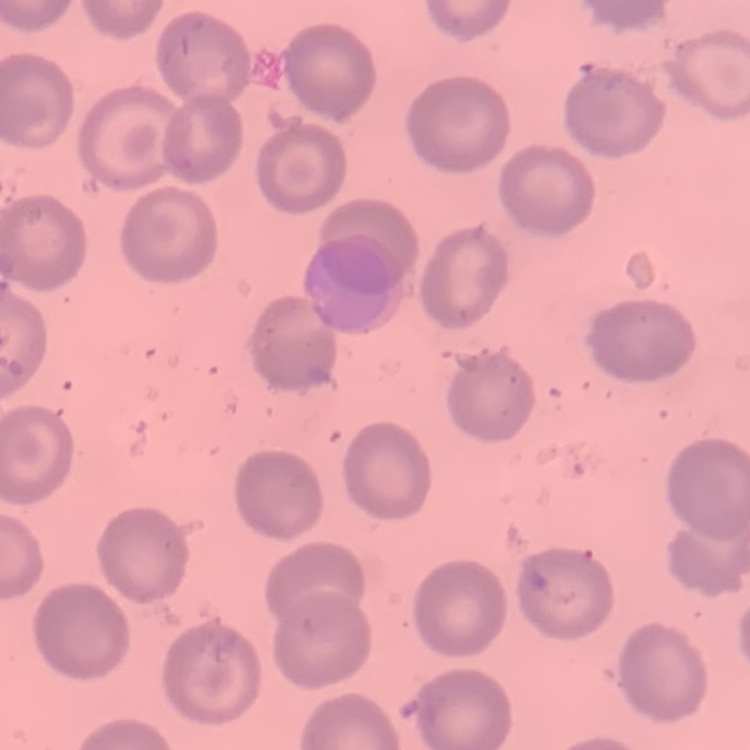 The red blood cells exhibit no rouleaux formation. Stained with either Field's or Giemsa. Thin peripheral smear. One tile cut from a larger photomicrograph.